Name the parasite shown.
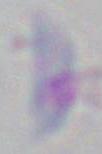

This is Toxoplasma gondii.

Micrograph. Captured at 1000x magnification.